Assess this cell for malaria.
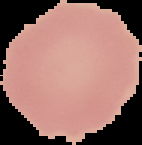

Uninfected.

Summary:
  - Preparation: thin blood smear
  - Image type: segmented cell region on a black background
  - Image size: 142×145 pixels